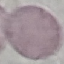

Malaria status: uninfected. Giemsa stain. Thin blood smear. Photographed with a smartphone camera at the microscope eyepiece. Automatically extracted cell patch, resized to 64 × 64 pixels.